Classify this cell by malaria status.
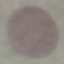

Uninfected.

stain = Giemsa
image type = automatically extracted cell patch, resized to 64 × 64 pixels
capture = smartphone through the microscope eyepiece
preparation = thin blood film